Identify the parasite.
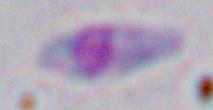

Toxoplasma gondii.

Summary:
  - Modality: photomicrograph
  - Magnification: 1000x